Outline platelets.
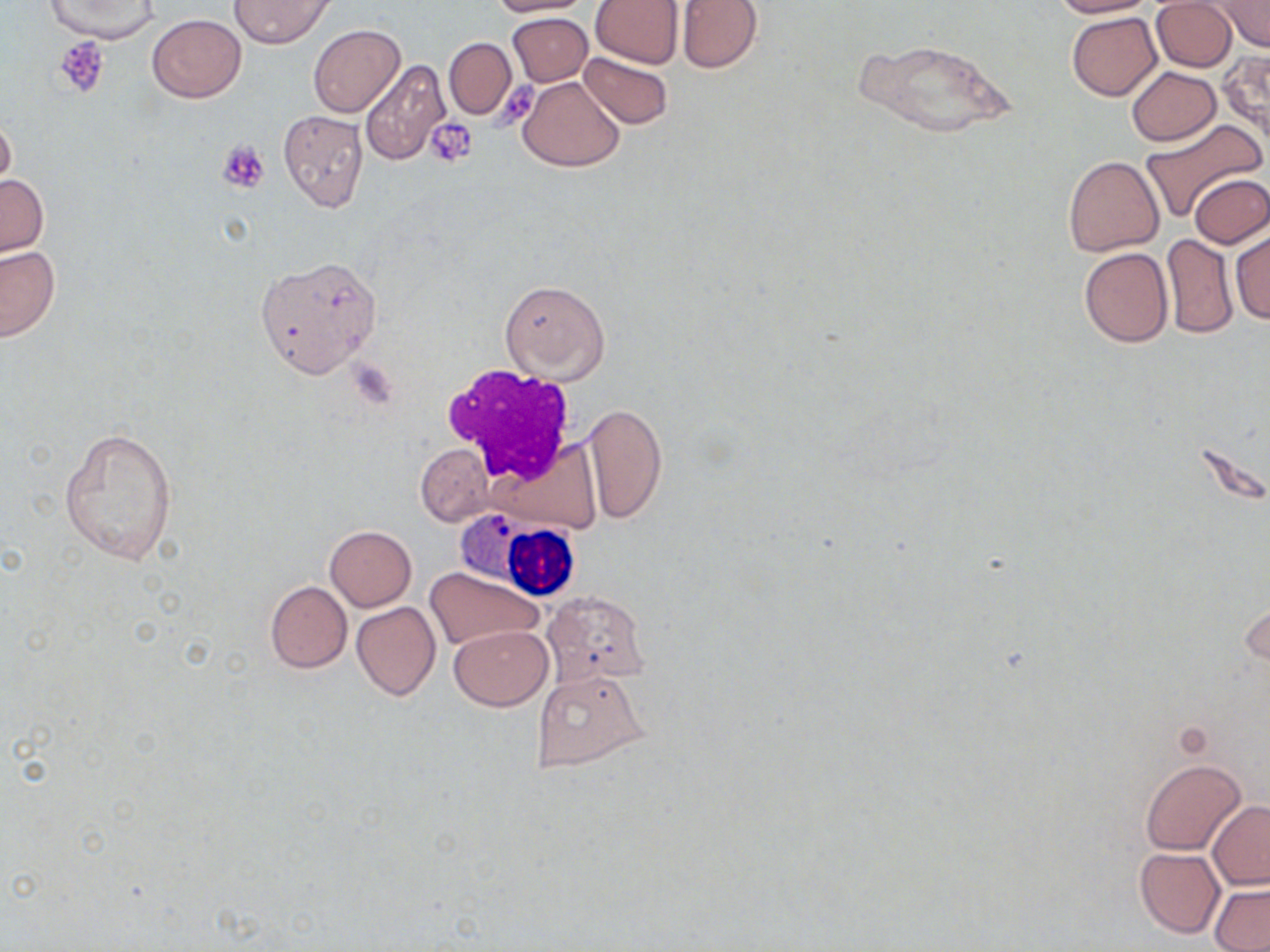
Approximate bounding boxes as [x1, y1, x2, y2] in pixels.
Platelets: [54, 38, 111, 99], [487, 78, 542, 139], [427, 117, 477, 166], [216, 139, 271, 195].

slide-level diagnosis = negative for blood parasites
preparation = thin blood film
magnification = 1000x
stain = May-Grünwald-Giemsa
field of view = one of a larger specimen
modality = light microscopy
white blood cell locations = approximate bounding boxes as [x1, y1, x2, y2] in pixels: [440, 363, 580, 484], [454, 510, 584, 600]
uninfected red blood cell locations = approximate bounding boxes as [x1, y1, x2, y2] in pixels: [229, 0, 334, 47], [487, 0, 591, 16], [591, 0, 684, 68], [675, 0, 762, 73], [1049, 0, 1159, 18], [1150, 0, 1237, 72], [46, 1, 158, 43], [1212, 2, 1270, 52], [508, 12, 592, 86], [1067, 13, 1161, 101], [147, 14, 246, 102], [309, 23, 404, 117], [443, 38, 516, 119], [857, 38, 1016, 139], [1216, 49, 1270, 148], [578, 50, 673, 130], [359, 59, 452, 168], [1125, 67, 1222, 146], [517, 75, 625, 172], [279, 109, 368, 211], [0, 114, 17, 195], [1140, 117, 1266, 224], [1062, 155, 1164, 256], [1189, 173, 1269, 248], [1, 174, 48, 257], [1230, 227, 1269, 325], [1161, 233, 1237, 339], [0, 246, 61, 342], [1078, 246, 1173, 348], [254, 256, 381, 378], [500, 279, 610, 381], [583, 402, 668, 525], [59, 426, 178, 566], [416, 443, 492, 525], [324, 525, 416, 610], [425, 567, 544, 652], [264, 580, 352, 673], [542, 591, 650, 684], [1242, 598, 1269, 673], [352, 602, 441, 701], [449, 625, 553, 710], [533, 669, 647, 773], [1141, 759, 1247, 855], [1206, 802, 1270, 890], [1135, 847, 1224, 939], [1210, 883, 1270, 952]
image size = 1270×952 pixels